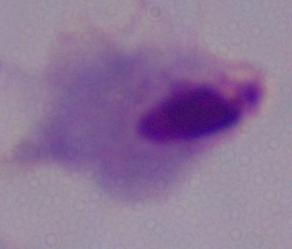

{
  "identification": "trichomonad",
  "magnification": "1000x",
  "modality": "micrograph"
}